Give the extent of all uninfected red blood cells.
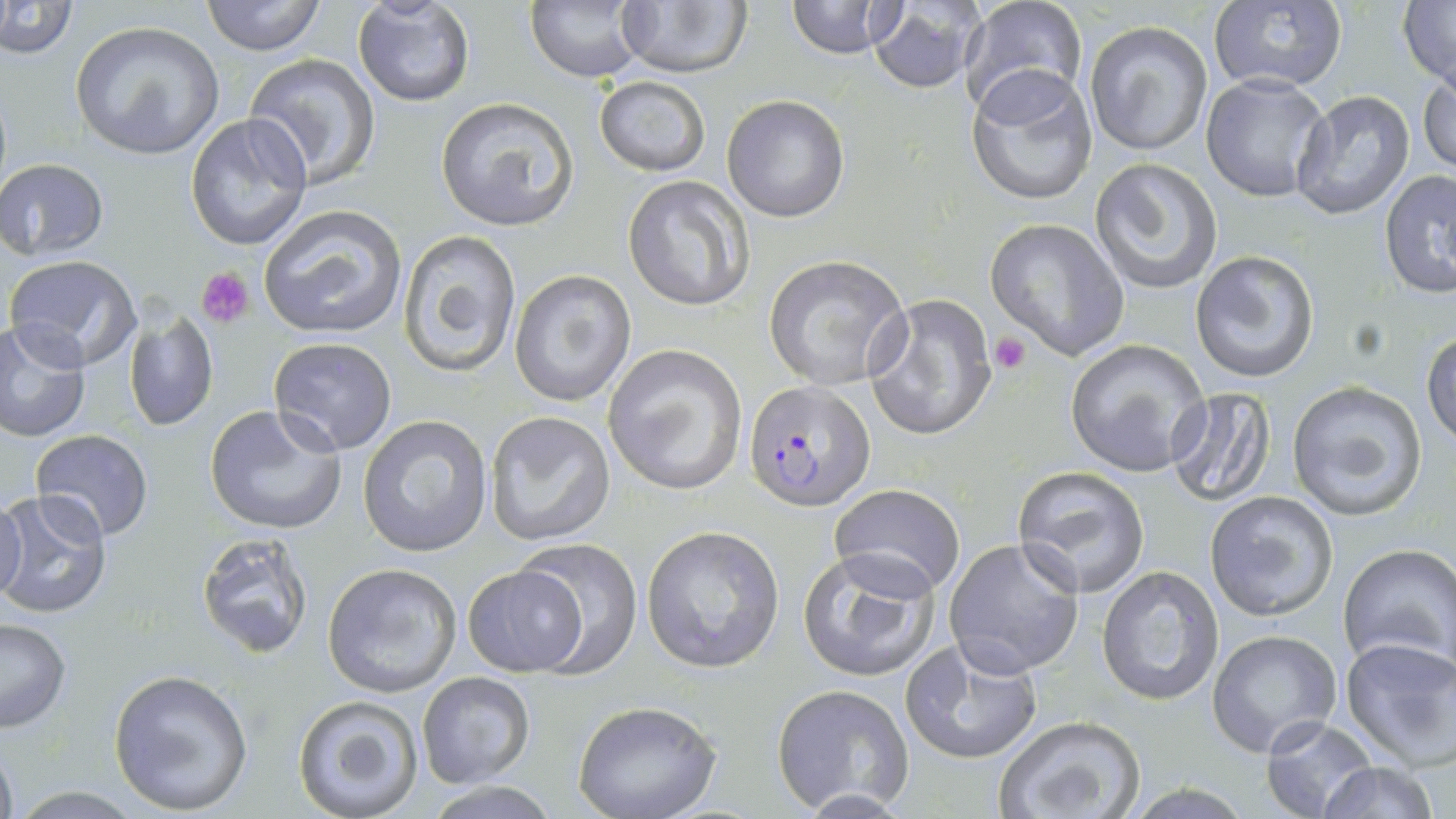
Approximate bounding boxes as (x1, y1, x2, y2) in pixels.
Uninfected red blood cells: (0, 0, 77, 58), (201, 0, 325, 56), (525, 0, 650, 84), (785, 0, 898, 59), (1207, 0, 1349, 94), (1399, 0, 1456, 90), (866, 1, 987, 93), (351, 2, 476, 109), (612, 2, 751, 81), (958, 2, 1088, 119), (70, 20, 225, 160), (1083, 20, 1214, 157), (244, 54, 383, 189), (966, 68, 1099, 207), (1418, 70, 1456, 178), (1201, 74, 1334, 204), (594, 75, 711, 176), (1290, 91, 1416, 219), (723, 94, 850, 222), (435, 97, 580, 231), (185, 113, 313, 254), (1089, 156, 1224, 296), (0, 157, 109, 262), (1379, 168, 1456, 301), (622, 176, 754, 312), (257, 204, 410, 340), (986, 218, 1129, 359), (397, 228, 523, 376), (1190, 250, 1320, 382), (6, 254, 141, 370), (763, 254, 912, 389), (510, 269, 637, 408), (868, 291, 999, 441), (124, 310, 219, 432), (0, 319, 93, 442), (1423, 327, 1456, 450), (267, 337, 398, 455), (1063, 338, 1211, 477), (602, 343, 748, 497), (1285, 380, 1429, 521), (1163, 387, 1276, 505), (204, 403, 351, 537), (484, 412, 616, 547), (357, 414, 493, 557), (29, 428, 155, 539), (1010, 466, 1151, 597), (829, 483, 967, 598), (1, 491, 114, 618), (0, 492, 27, 606), (1203, 492, 1339, 621), (641, 525, 786, 673), (193, 531, 315, 659), (943, 536, 1086, 678), (507, 540, 644, 674), (1336, 542, 1456, 676), (797, 548, 941, 681), (322, 562, 462, 697), (461, 563, 590, 677), (1095, 565, 1223, 707), (0, 616, 72, 734), (1207, 629, 1343, 760), (901, 637, 1044, 765), (1339, 637, 1456, 768), (108, 669, 254, 815), (416, 671, 535, 788), (770, 683, 916, 815), (293, 695, 425, 819), (571, 700, 720, 819), (992, 714, 1146, 819), (1261, 714, 1378, 819), (0, 735, 18, 819), (1316, 760, 1442, 819).

{
  "slide_level_diagnosis": "Plasmodium falciparum",
  "platelet_locations": "approximate bounding boxes as (x1, y1, x2, y2) in pixels: (197, 267, 253, 327), (990, 331, 1031, 374)",
  "field_of_view": "single",
  "preparation": "thin blood film",
  "modality": "optical microscopy",
  "stain": "May-Grünwald-Giemsa",
  "plasmodium_falciparum_infected_red_blood_cell_locations": "approximate bounding boxes as (x1, y1, x2, y2) in pixels: (745, 379, 878, 510)",
  "magnification": "1000x",
  "image_size": "1456×819 pixels"
}